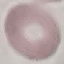

Malaria status: uninfected. Automatically extracted cell patch, resized to 64 × 64 pixels. Photographed with a smartphone camera at the microscope eyepiece. Giemsa stain. Thin blood smear.